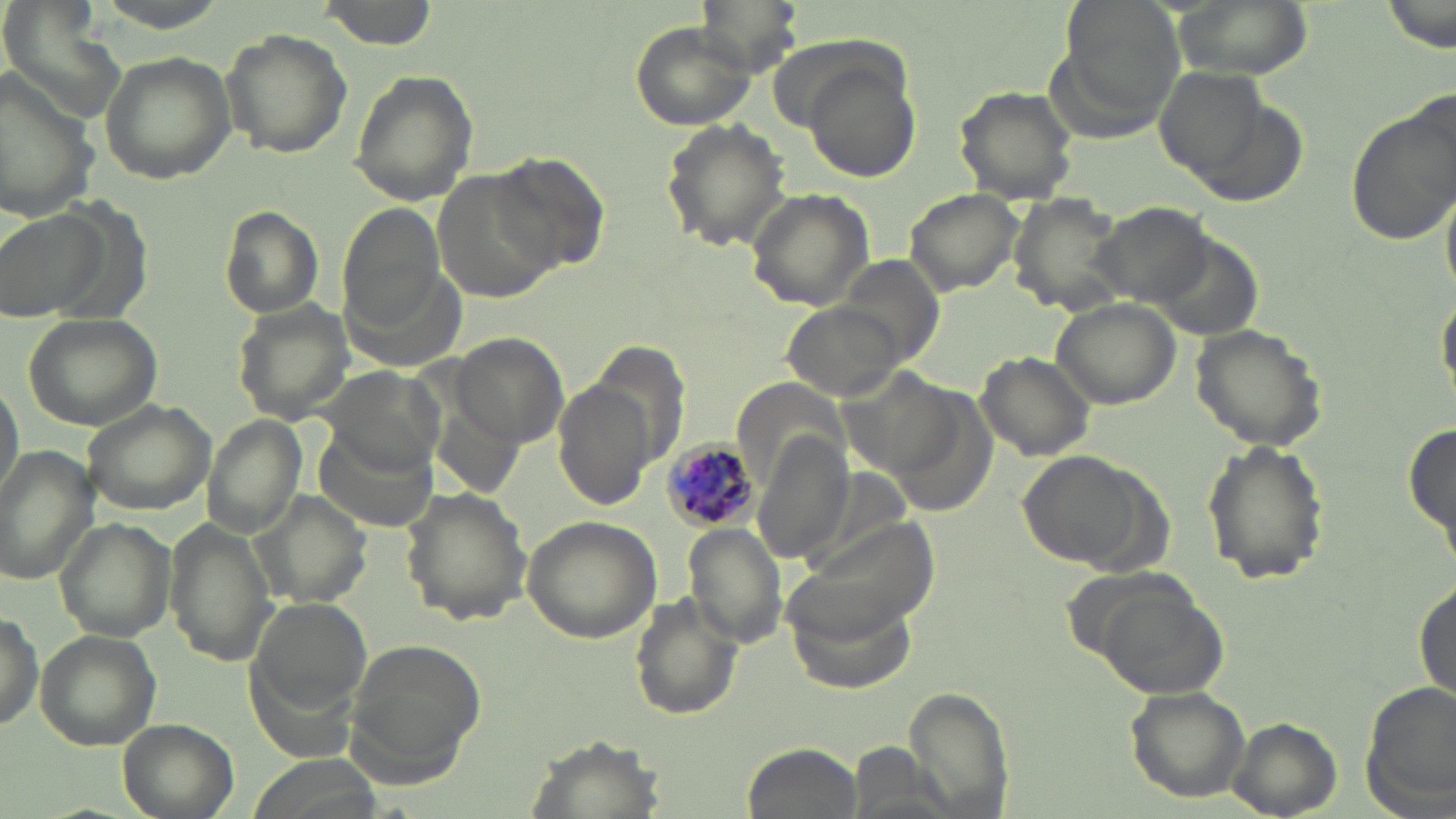
{
  "slide_level_diagnosis": "Plasmodium malariae",
  "preparation": "thin blood smear",
  "image_size": "1456×819 pixels",
  "modality": "light microscopy",
  "stain": "May-Grünwald-Giemsa",
  "plasmodium_malariae_infected_red_blood_cell_locations": "approximate bounding boxes as (x1,y1)-(x2,y2) corner pairs in pixels: (662,440)-(758,536)",
  "field_of_view": "one of a larger specimen",
  "magnification": "1000x",
  "uninfected_red_blood_cell_locations": "approximate bounding boxes as (x1,y1)-(x2,y2) corner pairs in pixels: (316,0)-(439,50), (693,0)-(804,76), (1165,0)-(1316,83), (1384,0)-(1454,54), (630,20)-(758,131), (221,27)-(351,158), (98,51)-(237,184), (805,59)-(922,184), (1155,66)-(1267,177), (349,69)-(478,206), (0,70)-(102,223), (954,86)-(1077,205), (1344,102)-(1454,246), (659,118)-(791,253), (482,151)-(614,277), (433,174)-(555,299), (903,186)-(1026,296), (747,190)-(875,310), (1008,195)-(1129,314), (1091,201)-(1215,303), (338,205)-(449,327), (218,207)-(325,320), (1,214)-(98,326), (841,257)-(945,369), (1436,287)-(1455,408), (1049,297)-(1183,408), (229,299)-(355,425), (783,302)-(907,400), (23,313)-(164,430), (1188,321)-(1329,453), (450,332)-(567,445), (974,350)-(1098,464), (318,365)-(446,477), (0,370)-(23,508), (554,379)-(659,512), (79,397)-(217,514), (200,415)-(309,538), (1404,418)-(1455,557), (314,423)-(440,533), (1198,438)-(1332,586), (756,441)-(852,563), (1,446)-(100,587), (1018,449)-(1155,570), (401,484)-(533,626), (254,490)-(373,607), (521,515)-(662,643), (55,518)-(177,644), (164,521)-(280,663), (684,523)-(788,648), (1414,579)-(1454,701), (784,580)-(921,692), (1093,580)-(1228,698), (628,592)-(740,720), (247,594)-(370,739), (1,614)-(43,733), (35,630)-(161,748), (343,642)-(484,780), (906,683)-(1014,817), (1360,684)-(1455,813), (1122,685)-(1255,803), (1225,716)-(1343,816), (117,717)-(240,819), (520,731)-(668,819), (741,742)-(865,819)"
}